Locate and identify every blood parasite.
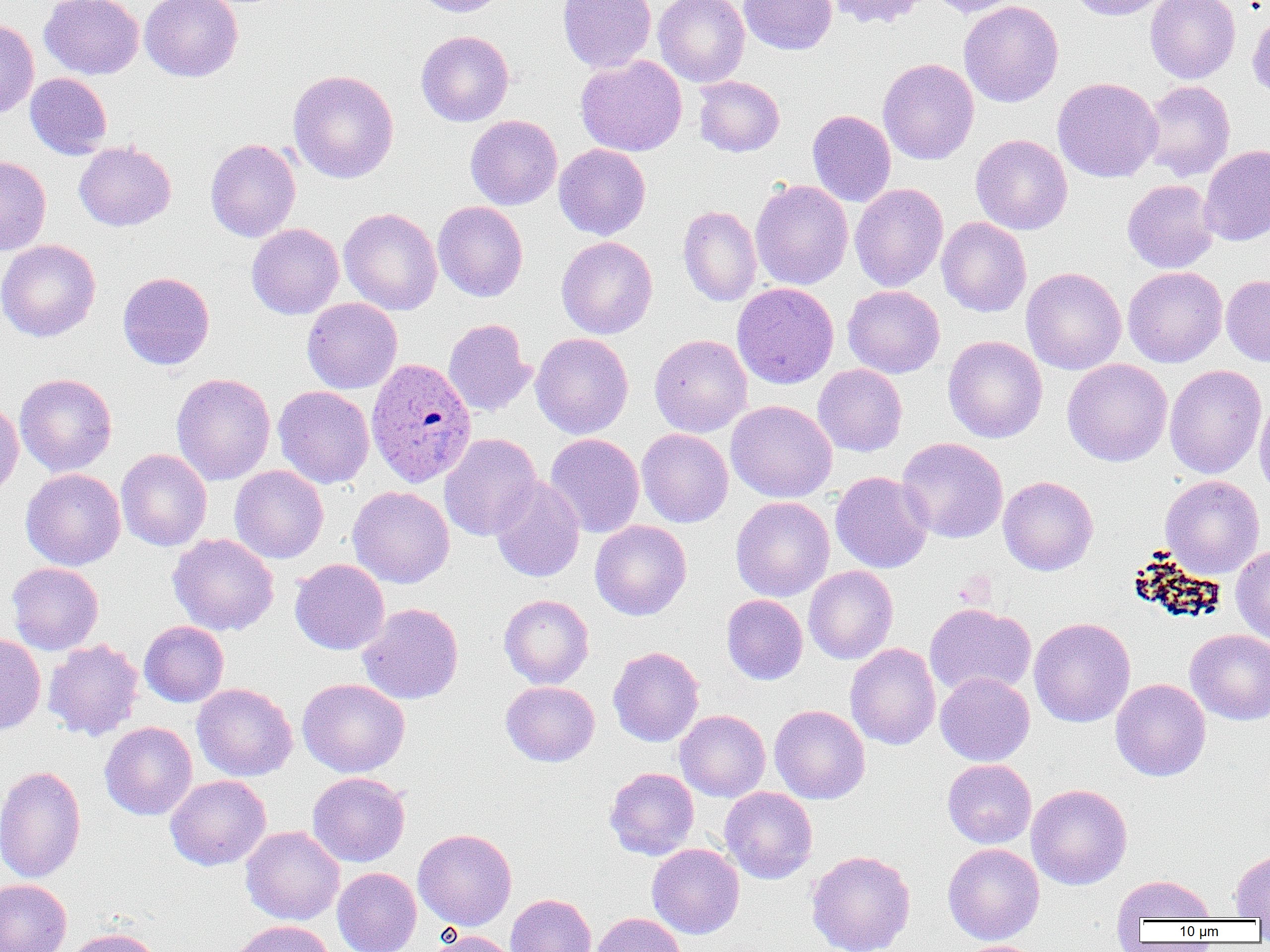
Approximate bounding boxes as named x1/y1/x2/y2 corners in pixels.
Plasmodium ovale-infected red blood cells: (x1=365, y1=360, x2=476, y2=495).
No Plasmodium falciparum, Plasmodium malariae, Plasmodium vivax, Babesia divergens, or Trypanosoma brucei observed.

Summary:
  - Uninfected red blood cell locations: (x1=40, y1=0, x2=144, y2=79), (x1=140, y1=0, x2=243, y2=82), (x1=412, y1=0, x2=510, y2=17), (x1=557, y1=0, x2=656, y2=73), (x1=654, y1=0, x2=750, y2=87), (x1=739, y1=0, x2=837, y2=55), (x1=825, y1=0, x2=928, y2=28), (x1=928, y1=0, x2=1025, y2=17), (x1=1067, y1=0, x2=1174, y2=21), (x1=1145, y1=0, x2=1241, y2=84), (x1=958, y1=1, x2=1063, y2=108), (x1=1247, y1=7, x2=1270, y2=100), (x1=0, y1=20, x2=39, y2=118), (x1=416, y1=30, x2=514, y2=127), (x1=575, y1=55, x2=687, y2=156), (x1=878, y1=58, x2=979, y2=165), (x1=288, y1=69, x2=399, y2=183), (x1=25, y1=72, x2=112, y2=159), (x1=694, y1=76, x2=785, y2=157), (x1=1052, y1=77, x2=1163, y2=183), (x1=1140, y1=80, x2=1236, y2=181), (x1=807, y1=110, x2=896, y2=207), (x1=465, y1=115, x2=563, y2=210), (x1=970, y1=134, x2=1073, y2=235), (x1=205, y1=138, x2=301, y2=242), (x1=74, y1=141, x2=176, y2=231), (x1=554, y1=143, x2=651, y2=240), (x1=1199, y1=145, x2=1270, y2=246), (x1=0, y1=156, x2=51, y2=255), (x1=750, y1=179, x2=853, y2=290), (x1=1122, y1=179, x2=1219, y2=274), (x1=849, y1=183, x2=949, y2=292), (x1=432, y1=201, x2=528, y2=302), (x1=677, y1=205, x2=762, y2=307), (x1=339, y1=207, x2=442, y2=315), (x1=936, y1=217, x2=1031, y2=317), (x1=246, y1=223, x2=344, y2=319), (x1=556, y1=236, x2=657, y2=339), (x1=0, y1=239, x2=100, y2=342), (x1=1123, y1=266, x2=1227, y2=367), (x1=1021, y1=267, x2=1126, y2=375), (x1=118, y1=271, x2=215, y2=370), (x1=1221, y1=274, x2=1270, y2=367), (x1=732, y1=282, x2=839, y2=389), (x1=842, y1=285, x2=945, y2=378), (x1=302, y1=297, x2=402, y2=394), (x1=443, y1=318, x2=536, y2=417), (x1=531, y1=332, x2=633, y2=439), (x1=649, y1=334, x2=752, y2=437), (x1=943, y1=335, x2=1047, y2=443), (x1=1062, y1=359, x2=1173, y2=466), (x1=813, y1=364, x2=907, y2=457), (x1=1164, y1=364, x2=1266, y2=479), (x1=171, y1=372, x2=276, y2=485), (x1=15, y1=373, x2=117, y2=476), (x1=273, y1=385, x2=374, y2=488), (x1=1254, y1=393, x2=1270, y2=502), (x1=0, y1=400, x2=24, y2=499), (x1=725, y1=400, x2=837, y2=503), (x1=636, y1=428, x2=734, y2=528), (x1=440, y1=432, x2=541, y2=541), (x1=545, y1=433, x2=645, y2=537), (x1=896, y1=437, x2=1008, y2=543), (x1=116, y1=449, x2=212, y2=551), (x1=229, y1=465, x2=329, y2=563), (x1=21, y1=468, x2=126, y2=570), (x1=831, y1=472, x2=933, y2=573), (x1=1161, y1=474, x2=1264, y2=578), (x1=998, y1=475, x2=1098, y2=576), (x1=489, y1=476, x2=585, y2=583), (x1=348, y1=485, x2=454, y2=588), (x1=730, y1=496, x2=834, y2=601), (x1=590, y1=520, x2=692, y2=620), (x1=167, y1=532, x2=279, y2=636), (x1=1231, y1=545, x2=1270, y2=645), (x1=290, y1=558, x2=390, y2=655), (x1=7, y1=562, x2=104, y2=655), (x1=804, y1=565, x2=898, y2=664), (x1=721, y1=594, x2=808, y2=685), (x1=499, y1=595, x2=594, y2=689), (x1=357, y1=603, x2=463, y2=704), (x1=924, y1=603, x2=1036, y2=698), (x1=1029, y1=617, x2=1136, y2=727), (x1=139, y1=620, x2=229, y2=707), (x1=1185, y1=629, x2=1270, y2=725), (x1=0, y1=634, x2=46, y2=736), (x1=42, y1=639, x2=144, y2=741), (x1=845, y1=643, x2=941, y2=750), (x1=608, y1=647, x2=704, y2=747), (x1=935, y1=672, x2=1035, y2=766), (x1=297, y1=677, x2=410, y2=777), (x1=1110, y1=678, x2=1211, y2=781), (x1=501, y1=681, x2=600, y2=766), (x1=192, y1=683, x2=297, y2=781), (x1=769, y1=704, x2=870, y2=804), (x1=675, y1=710, x2=771, y2=801), (x1=99, y1=721, x2=198, y2=820), (x1=942, y1=759, x2=1037, y2=848), (x1=0, y1=764, x2=87, y2=883), (x1=605, y1=767, x2=699, y2=860), (x1=307, y1=772, x2=410, y2=867), (x1=165, y1=774, x2=271, y2=870), (x1=1026, y1=784, x2=1132, y2=890), (x1=720, y1=787, x2=817, y2=884), (x1=241, y1=826, x2=344, y2=925), (x1=413, y1=828, x2=517, y2=931), (x1=646, y1=843, x2=745, y2=939), (x1=943, y1=843, x2=1045, y2=945), (x1=806, y1=849, x2=916, y2=952), (x1=1230, y1=849, x2=1270, y2=919), (x1=332, y1=867, x2=421, y2=952), (x1=1112, y1=875, x2=1218, y2=925), (x1=0, y1=878, x2=72, y2=952), (x1=506, y1=893, x2=596, y2=952), (x1=590, y1=912, x2=687, y2=952), (x1=226, y1=920, x2=335, y2=952), (x1=64, y1=927, x2=164, y2=952), (x1=427, y1=929, x2=521, y2=952), (x1=949, y1=940, x2=1045, y2=952)
  - Slide-level diagnosis: Plasmodium ovale
  - Preparation: thin blood film
  - Image size: 1270×952 pixels
  - Magnification: 1000x
  - Modality: optical microscopy
  - Field of view: one of a larger specimen